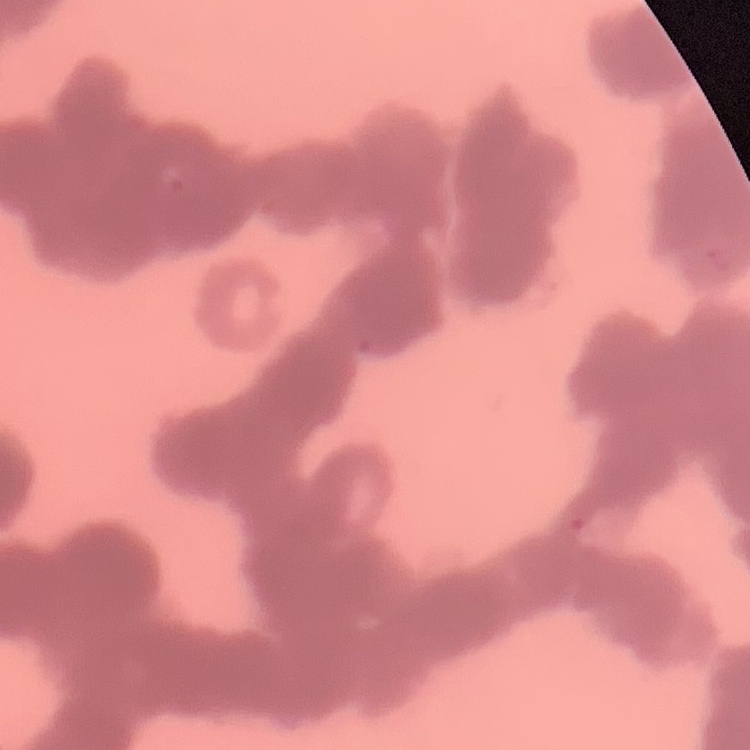

red blood cell morphology = rouleaux formation
preparation = thin blood smear
image type = one tile cut from a larger photomicrograph
stain = Field's or Giemsa